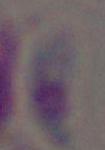
Summary:
  - Identification: Toxoplasma gondii
  - Modality: micrograph
  - Magnification: 1000x